Assess this cell for malaria.
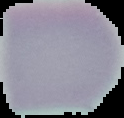
Uninfected.

{
  "image_type": "cell region segmented out of the field of view; surrounding area masked to black",
  "preparation": "thin blood film",
  "image_size": "124×118 pixels"
}